Give the position of every leukocyte visible.
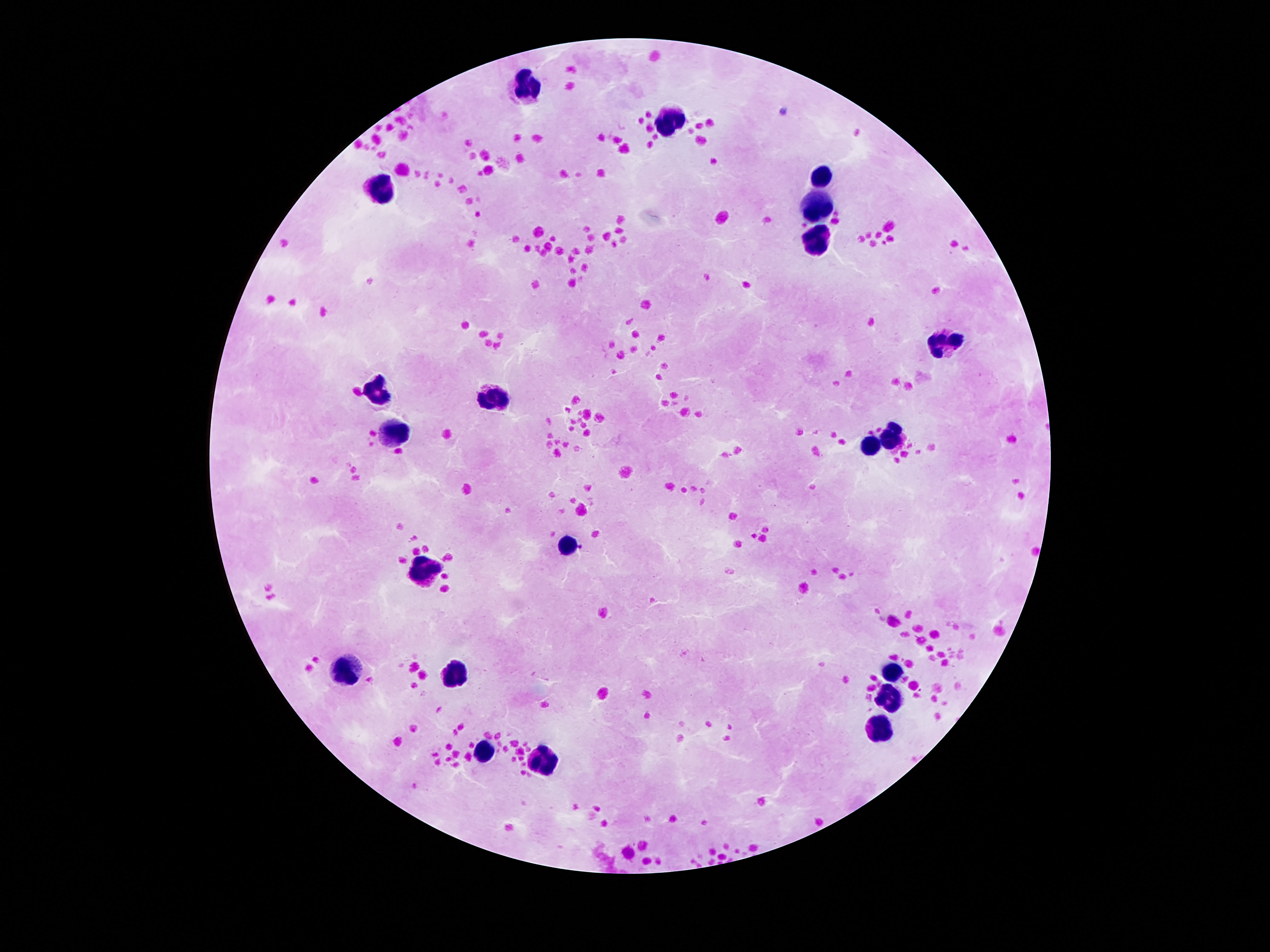
Approximate centers as {x, y} in pixels.
Leukocytes: {528, 85}, {674, 121}, {821, 176}, {386, 189}, {814, 212}, {823, 243}, {944, 344}, {377, 393}, {493, 397}, {392, 434}, {892, 436}, {870, 445}, {567, 546}, {427, 572}, {347, 670}, {457, 673}, {892, 673}, {890, 696}, {879, 731}, {483, 750}, {545, 758}.

Summary:
  - Stain: Giemsa
  - Field of view: single
  - Image size: 1270×952 pixels
  - Patient malaria status: negative
  - Preparation: thick peripheral-blood smear
  - Magnification: 100x
  - Capture: smartphone camera through the microscope eyepiece